Point out each Plasmodium parasite.
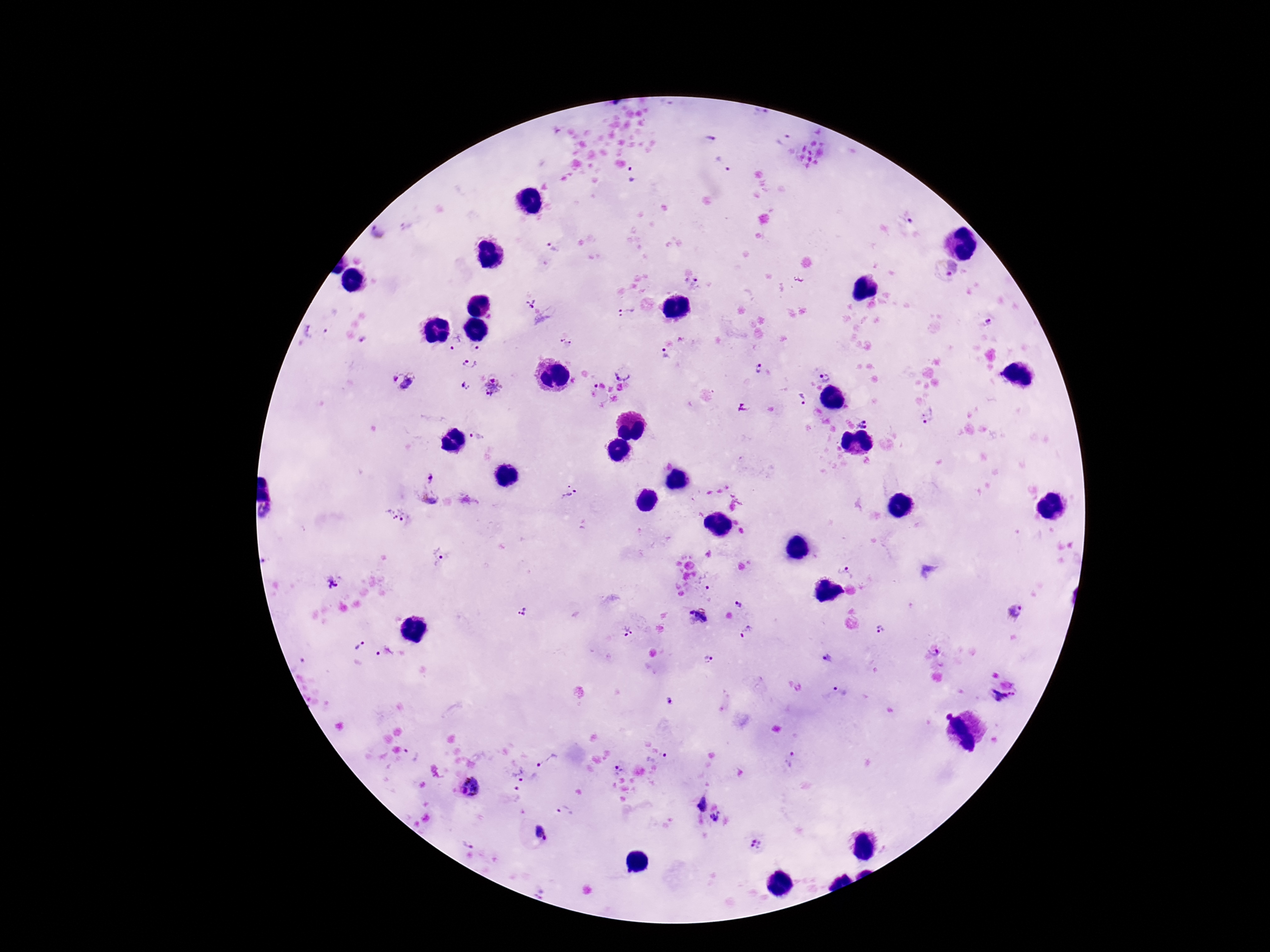
Approximate centers as {x, y} in pixels.
Plasmodium parasites: {710, 138}, {723, 165}, {632, 176}, {911, 221}, {553, 247}, {946, 268}, {691, 284}, {531, 304}, {627, 312}, {331, 320}, {988, 322}, {308, 331}, {363, 338}, {565, 341}, {455, 343}, {475, 348}, {665, 354}, {470, 364}, {758, 368}, {624, 370}, {824, 378}, {402, 382}, {465, 386}, {594, 386}, {493, 387}, {620, 387}, {802, 399}, {928, 417}, {863, 424}, {477, 436}, {430, 478}, {568, 492}, {396, 515}, {439, 555}, {845, 570}, {334, 583}, {708, 587}, {738, 603}, {522, 611}, {1014, 611}, {699, 615}, {882, 630}, {627, 631}, {747, 633}, {362, 645}, {384, 652}, {934, 653}, {708, 658}, {827, 659}, {297, 665}, {835, 693}, {1002, 702}, {411, 755}, {664, 756}, {791, 758}, {547, 760}, {618, 769}, {518, 774}, {471, 787}, {518, 794}, {700, 803}, {565, 811}, {716, 817}, {541, 832}, {469, 842}, {757, 843}.

Summary:
  - Magnification: 100x
  - Capture: smartphone camera through the microscope eyepiece
  - Image size: 1270×952 pixels
  - Preparation: thick blood film
  - Field of view: one from this slide
  - Patient malaria status: infected
  - Stain: Giemsa